Outline each uninfected red blood cell.
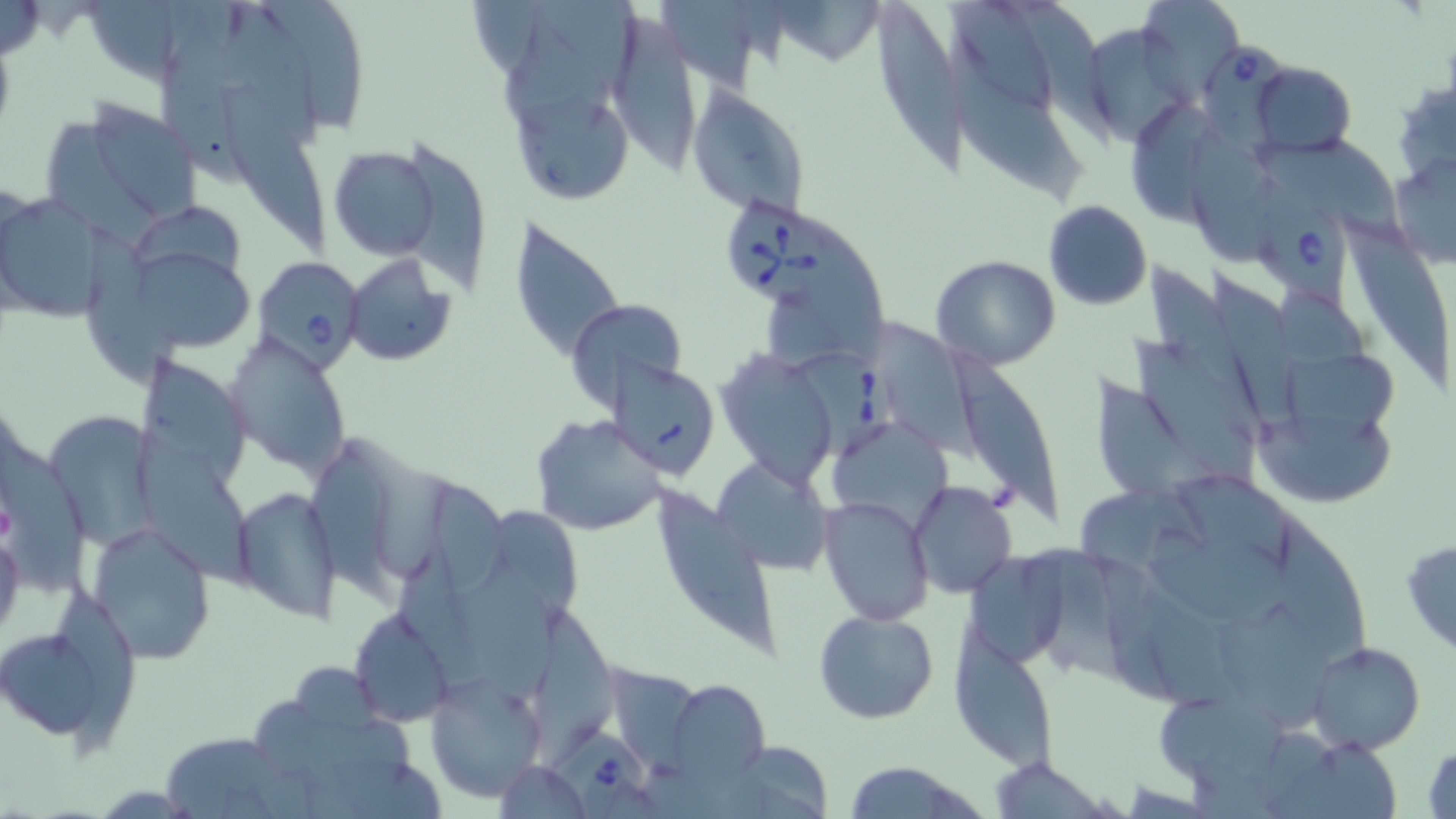

Approximate bounding boxes as [x1, y1, x2, y2] in pixels.
Uninfected red blood cells: [257, 0, 370, 137], [949, 0, 1055, 119], [1137, 0, 1246, 104], [653, 1, 771, 100], [873, 1, 976, 182], [498, 13, 621, 150], [604, 16, 708, 183], [1087, 21, 1202, 147], [949, 36, 1091, 211], [158, 44, 272, 189], [1250, 62, 1357, 157], [1392, 77, 1456, 188], [224, 86, 337, 269], [688, 87, 809, 220], [53, 96, 205, 231], [512, 97, 635, 207], [1123, 100, 1223, 221], [1185, 128, 1285, 265], [400, 141, 491, 301], [329, 145, 442, 261], [1387, 153, 1456, 270], [0, 193, 108, 322], [1043, 200, 1151, 310], [131, 207, 247, 308], [1339, 209, 1454, 382], [512, 214, 629, 362], [78, 221, 189, 394], [341, 254, 457, 366], [132, 255, 255, 361], [932, 255, 1058, 370], [1153, 266, 1264, 438], [1212, 272, 1324, 436], [565, 298, 688, 414], [874, 320, 992, 470], [226, 333, 352, 475], [1131, 340, 1264, 494], [946, 349, 1066, 532], [715, 350, 840, 489], [1290, 353, 1397, 459], [608, 359, 719, 478], [1082, 367, 1207, 512], [1249, 410, 1400, 507], [533, 414, 668, 536], [47, 419, 180, 562], [137, 435, 260, 597], [307, 457, 407, 603], [714, 458, 834, 574], [908, 481, 1017, 598], [649, 483, 781, 655], [230, 484, 341, 622], [432, 484, 510, 605], [1070, 485, 1228, 577], [821, 495, 932, 624], [1269, 515, 1376, 669], [90, 524, 216, 665], [0, 529, 25, 642], [1145, 534, 1316, 630], [1401, 538, 1456, 656], [963, 548, 1076, 672], [452, 565, 557, 709], [1210, 596, 1336, 737], [535, 606, 621, 772], [349, 608, 457, 728], [813, 608, 939, 724], [0, 616, 124, 747], [953, 633, 1057, 771], [1306, 640, 1428, 755], [425, 674, 546, 803], [666, 677, 771, 786], [1158, 693, 1291, 799], [159, 730, 289, 817], [1283, 738, 1402, 819], [1423, 740, 1455, 819], [989, 757, 1110, 816], [495, 760, 590, 818], [841, 764, 986, 819].

Summary:
  - Babesia divergens-infected red blood cell locations: [1200, 47, 1300, 155], [1255, 175, 1352, 326], [723, 196, 839, 319], [257, 259, 366, 381], [787, 354, 899, 469], [540, 728, 652, 819]
  - Platelet locations: [0, 500, 15, 545]
  - Slide-level diagnosis: Babesia divergens
  - Modality: optical microscopy
  - Magnification: 1000x
  - Field of view: one of a larger specimen
  - Image size: 1456×819 pixels
  - Preparation: thin blood smear
  - Stain: May-Grünwald-Giemsa